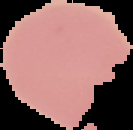 From a thin blood smear. Cell region segmented out of the field of view; the surrounding area is masked to black. Image is 133×130 pixels. Result: negative for Plasmodium parasites.